Locate every Plasmodium falciparum-infected red blood cell.
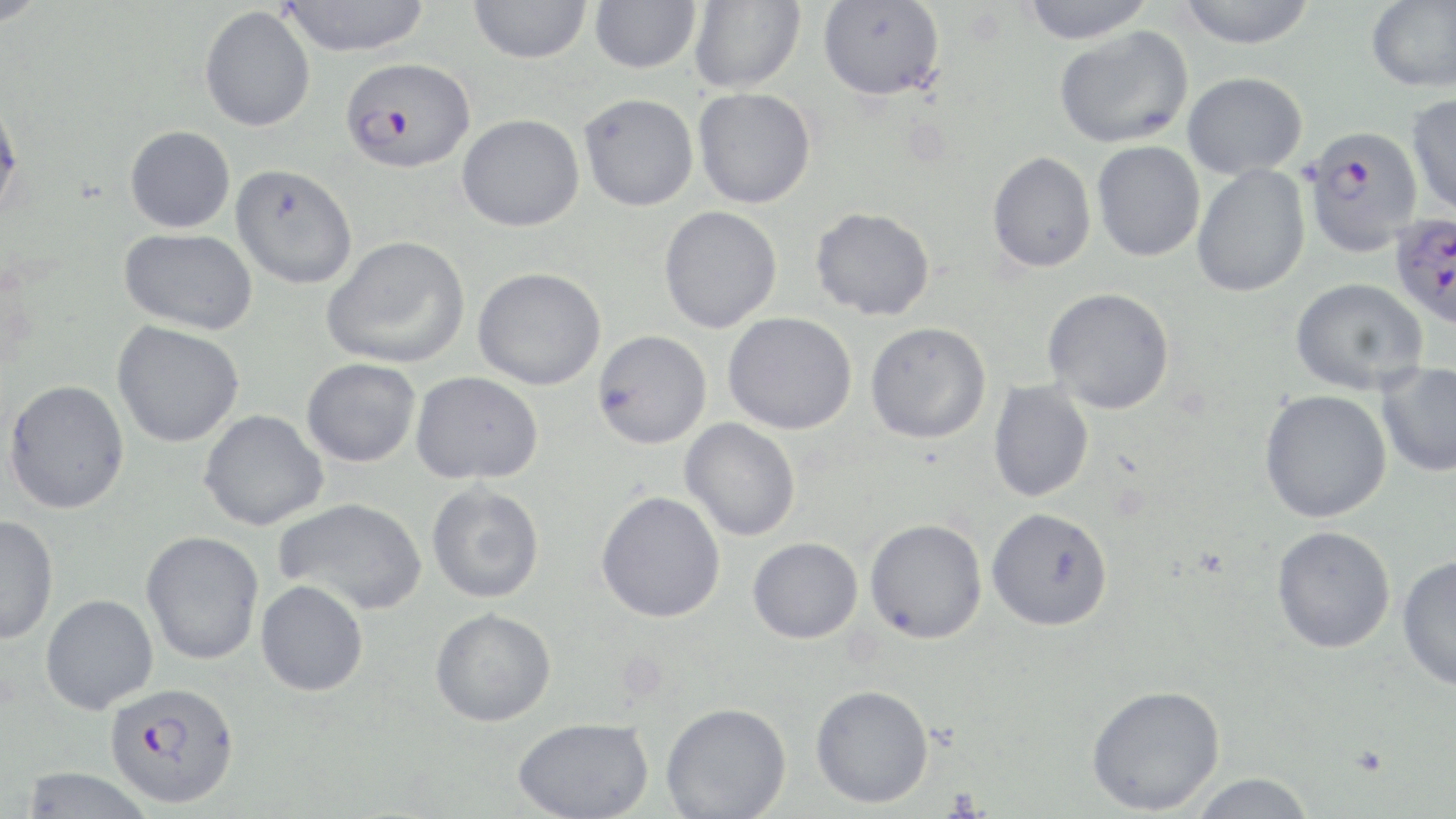

Approximate bounding boxes as [x1, y1, x2, y2] in pixels.
Plasmodium falciparum-infected red blood cells: [340, 57, 474, 172], [1303, 125, 1423, 257], [1390, 213, 1456, 330], [105, 681, 240, 809].

Summary:
  - Uninfected red blood cell locations: [0, 0, 50, 28], [279, 0, 432, 56], [589, 0, 701, 73], [689, 0, 805, 93], [1017, 0, 1159, 43], [1174, 0, 1319, 48], [1366, 0, 1456, 93], [468, 1, 592, 64], [818, 1, 946, 101], [200, 6, 316, 132], [1054, 25, 1194, 149], [1182, 72, 1308, 180], [693, 87, 816, 208], [1406, 92, 1456, 219], [0, 93, 25, 221], [579, 93, 699, 211], [457, 113, 585, 232], [125, 125, 235, 233], [1092, 141, 1205, 262], [987, 151, 1096, 273], [230, 164, 358, 289], [1191, 166, 1310, 297], [659, 206, 783, 333], [810, 207, 935, 320], [119, 228, 257, 335], [321, 235, 470, 369], [473, 267, 606, 390], [1290, 277, 1429, 395], [1043, 287, 1175, 414], [723, 312, 857, 435], [112, 321, 244, 448], [865, 322, 991, 444], [593, 329, 712, 449], [301, 358, 421, 468], [1377, 362, 1456, 478], [411, 371, 543, 485], [4, 379, 129, 514], [987, 381, 1094, 502], [1259, 390, 1392, 523], [199, 410, 328, 530], [680, 418, 801, 541], [427, 483, 545, 603], [596, 490, 726, 623], [275, 497, 427, 616], [987, 507, 1113, 631], [0, 514, 58, 645], [864, 518, 987, 643], [1271, 525, 1396, 654], [140, 530, 264, 665], [748, 537, 863, 644], [1397, 555, 1456, 690], [255, 579, 369, 696], [40, 594, 158, 714], [430, 608, 556, 727], [810, 684, 934, 808], [1086, 684, 1225, 815], [661, 702, 792, 819], [512, 717, 653, 819], [19, 767, 154, 818], [1187, 772, 1317, 819]
  - Slide-level diagnosis: Plasmodium falciparum
  - Preparation: thin blood film
  - Modality: optical microscopy
  - Image size: 1456×819 pixels
  - Stain: May-Grünwald-Giemsa
  - Field of view: single
  - Magnification: 1000x